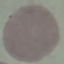

malaria_status: uninfected
image_type: cell patch, automatically extracted from a larger field of view and resized to 64 × 64 pixels
preparation: thin smear
capture: smartphone through the microscope eyepiece
stain: Giemsa